Classify this cell by malaria status.
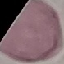
Uninfected.

preparation = thin blood film
capture = smartphone through the microscope eyepiece
stain = Giemsa
image type = automatically extracted cell patch, resized to 64 × 64 pixels